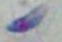

{
  "identification": "Toxoplasma gondii",
  "magnification": "1000x",
  "modality": "photomicrograph"
}